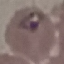

Result: malaria parasites identified. Thin blood smear. Photographed with a smartphone camera at the microscope eyepiece. Cell patch, automatically extracted from a larger field of view and resized to 64 × 64 pixels. Giemsa stain.